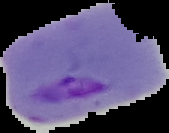

{
  "image_size": "169×133 pixels",
  "malaria_status": "parasitized",
  "preparation": "thin blood film",
  "image_type": "cell region segmented out of the field of view; surrounding area masked to black"
}